Report the malaria status of this cell.
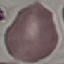

Uninfected.

image type = cell patch, automatically extracted from a larger field of view and resized to 64 × 64 pixels
stain = Giemsa
capture = smartphone through the microscope eyepiece
preparation = thin blood film